Outline each uninfected red blood cell.
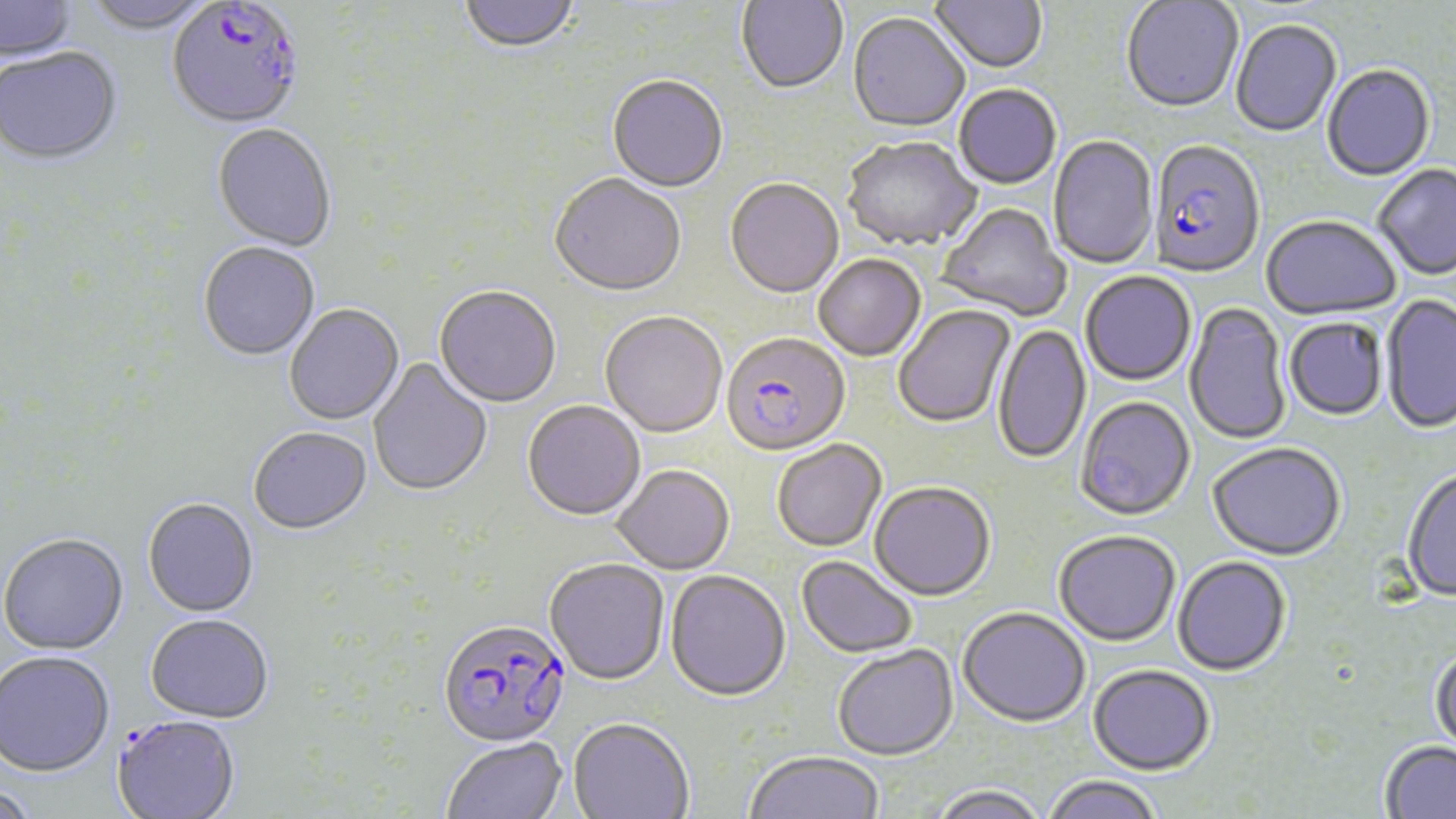
Approximate bounding boxes as named x1/y1/x2/y2 corners in pixels.
Uninfected red blood cells: (x1=81, y1=0, x2=216, y2=36), (x1=459, y1=0, x2=580, y2=55), (x1=736, y1=0, x2=848, y2=95), (x1=930, y1=0, x2=1047, y2=76), (x1=0, y1=1, x2=79, y2=64), (x1=1121, y1=1, x2=1244, y2=116), (x1=847, y1=15, x2=970, y2=134), (x1=1230, y1=21, x2=1342, y2=139), (x1=0, y1=50, x2=122, y2=168), (x1=1322, y1=66, x2=1436, y2=183), (x1=607, y1=77, x2=728, y2=194), (x1=954, y1=86, x2=1061, y2=191), (x1=212, y1=126, x2=336, y2=253), (x1=1049, y1=135, x2=1158, y2=270), (x1=843, y1=139, x2=981, y2=253), (x1=1373, y1=165, x2=1456, y2=282), (x1=549, y1=176, x2=687, y2=300), (x1=726, y1=180, x2=844, y2=301), (x1=936, y1=204, x2=1070, y2=322), (x1=1261, y1=217, x2=1401, y2=322), (x1=198, y1=244, x2=320, y2=362), (x1=813, y1=256, x2=926, y2=363), (x1=1080, y1=272, x2=1196, y2=387), (x1=434, y1=288, x2=561, y2=410), (x1=1380, y1=294, x2=1456, y2=436), (x1=1183, y1=302, x2=1291, y2=446), (x1=894, y1=305, x2=1016, y2=430), (x1=285, y1=306, x2=404, y2=426), (x1=600, y1=313, x2=727, y2=440), (x1=1284, y1=318, x2=1388, y2=422), (x1=993, y1=323, x2=1092, y2=467), (x1=368, y1=357, x2=493, y2=498), (x1=1075, y1=397, x2=1196, y2=523), (x1=522, y1=402, x2=645, y2=523), (x1=248, y1=428, x2=372, y2=536), (x1=772, y1=441, x2=887, y2=554), (x1=1207, y1=445, x2=1346, y2=563), (x1=611, y1=467, x2=734, y2=576), (x1=1402, y1=470, x2=1456, y2=604), (x1=869, y1=483, x2=995, y2=603), (x1=143, y1=499, x2=258, y2=618), (x1=0, y1=533, x2=128, y2=655), (x1=1053, y1=533, x2=1181, y2=649), (x1=796, y1=557, x2=918, y2=659), (x1=1172, y1=558, x2=1292, y2=678), (x1=544, y1=560, x2=669, y2=687), (x1=664, y1=572, x2=791, y2=705), (x1=957, y1=610, x2=1091, y2=730), (x1=145, y1=615, x2=274, y2=723), (x1=833, y1=647, x2=958, y2=763), (x1=1429, y1=647, x2=1456, y2=762), (x1=0, y1=651, x2=115, y2=776), (x1=1088, y1=667, x2=1215, y2=778), (x1=568, y1=719, x2=693, y2=819), (x1=441, y1=738, x2=567, y2=819), (x1=1379, y1=742, x2=1456, y2=819), (x1=744, y1=753, x2=884, y2=819), (x1=1041, y1=777, x2=1163, y2=819), (x1=0, y1=783, x2=42, y2=819), (x1=928, y1=787, x2=1049, y2=819).

Plasmodium falciparum-infected red blood cell locations: (x1=167, y1=1, x2=305, y2=133), (x1=1148, y1=142, x2=1265, y2=280), (x1=721, y1=335, x2=850, y2=460), (x1=437, y1=619, x2=571, y2=749), (x1=112, y1=714, x2=241, y2=819). Slide-level diagnosis: Plasmodium falciparum. Optical microscopy. Image is 1456×819 pixels. Captured at 1000x magnification. One field of a larger specimen. Thin blood film. May-Grünwald-Giemsa-stained preparation.